Describe the morphology of the erythrocytes.
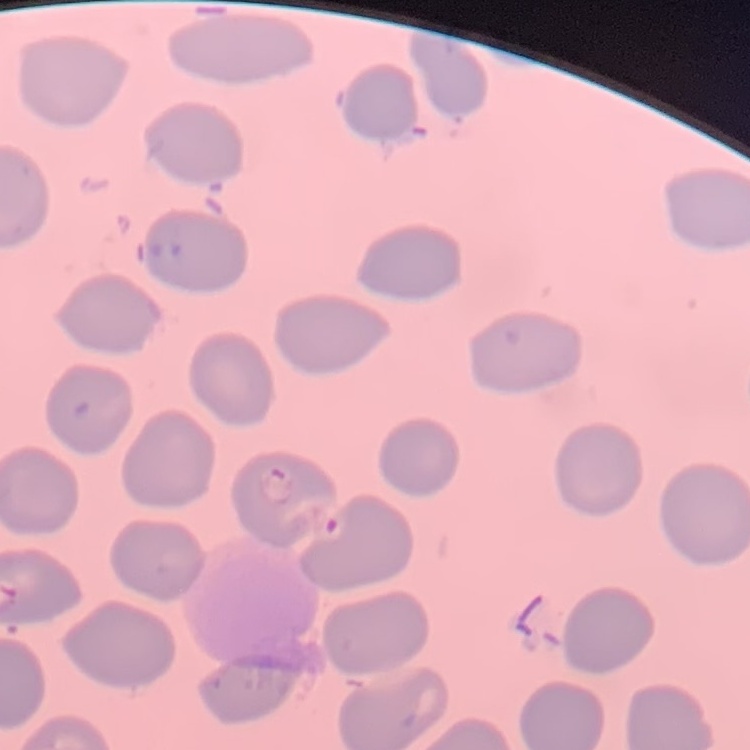

They show no rouleaux formation.

preparation = thin blood film
image type = square crop of a larger photomicrograph
stain = Field's or Giemsa